Assess for Plasmodium parasites.
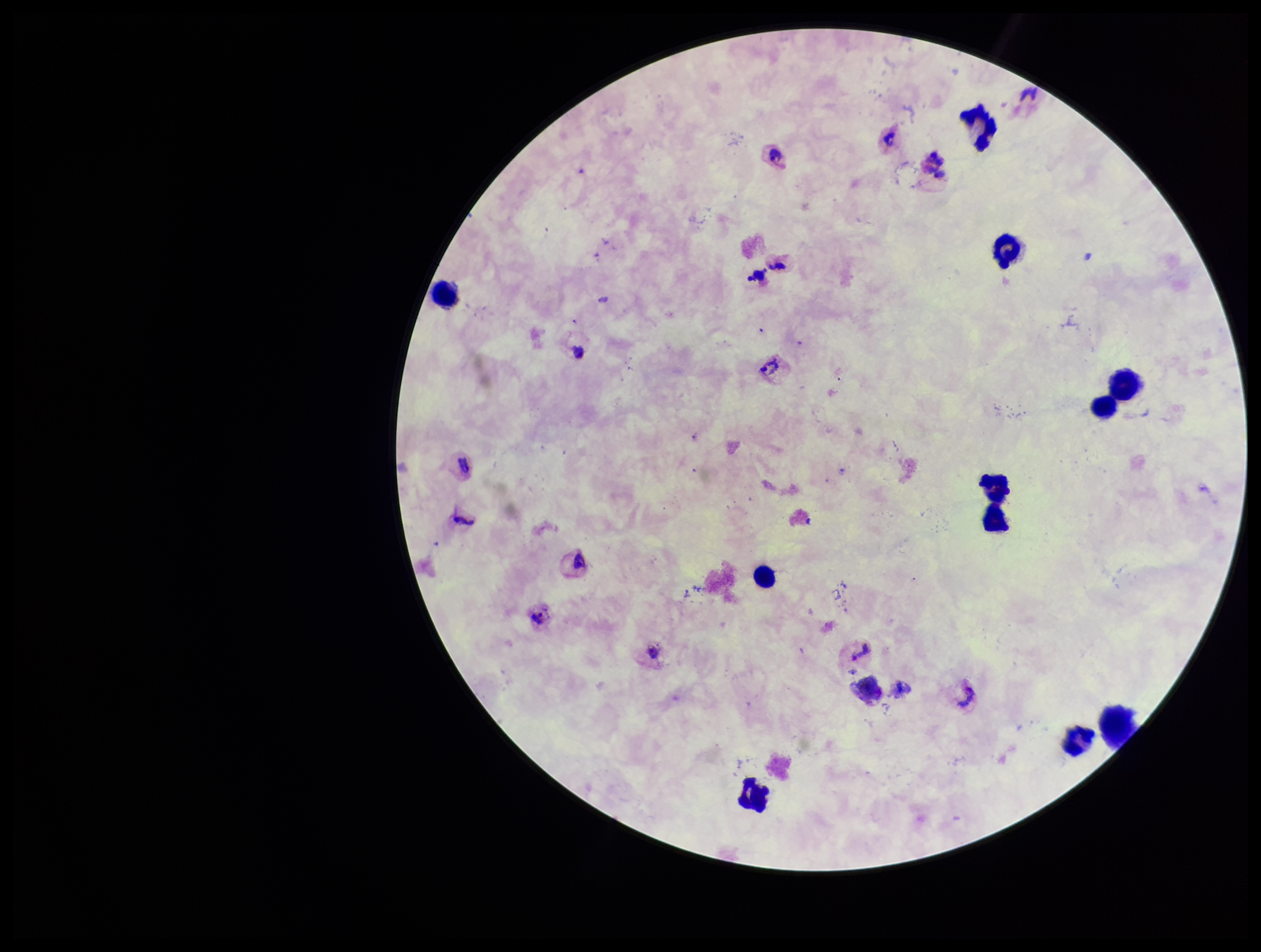
Detected.

Preparation: thick smear. Giemsa stain. Species reported for this patient: Plasmodium vivax. Leukocyte count: 10. Image is 1261×952 pixels. Parasite count: 4. One field from this slide. Patient malaria status: infected. Photographed through the microscope eyepiece with a smartphone camera.